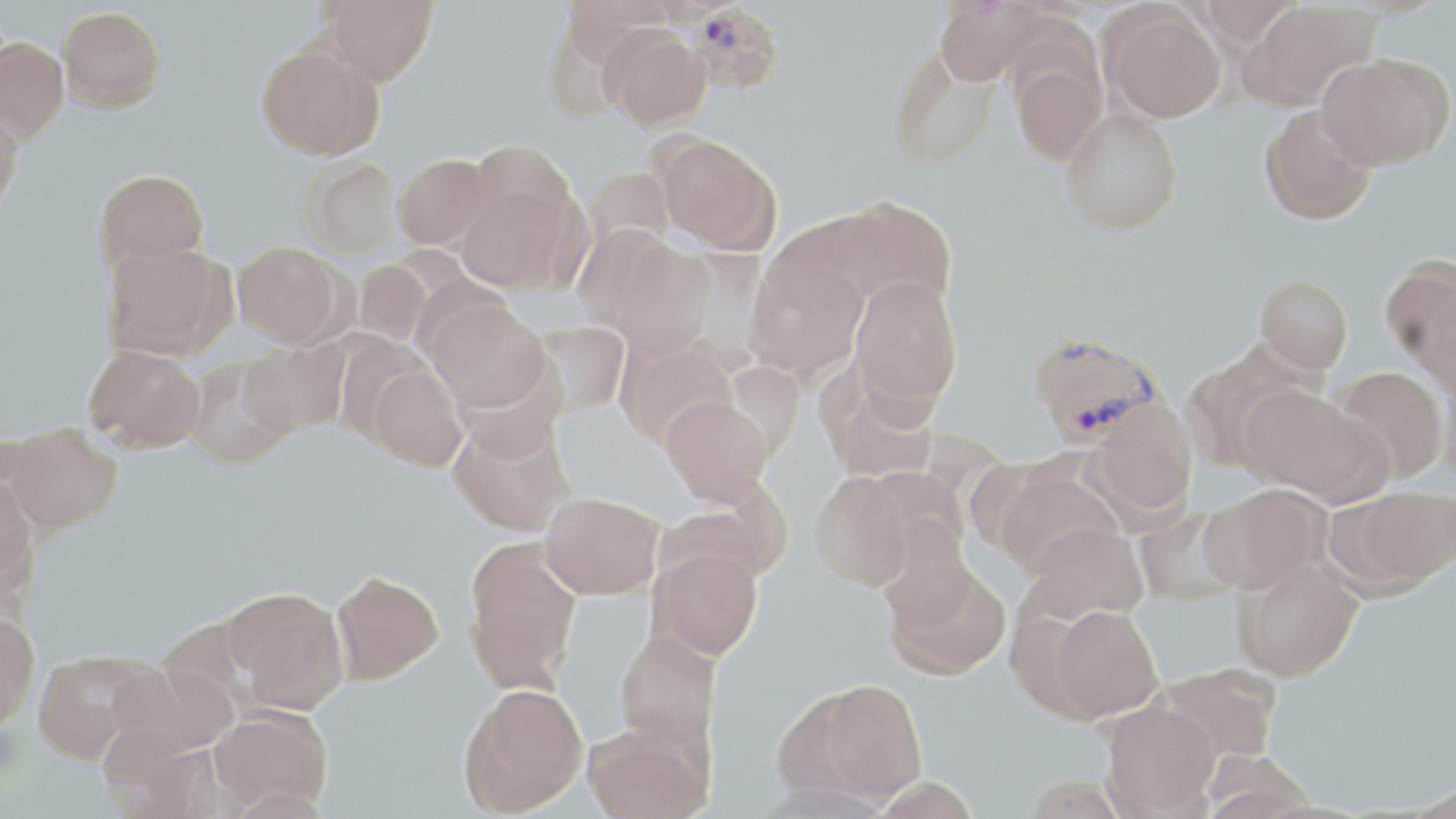

Plasmodium vivax-infected red blood cell locations = approximate bounding boxes as named x1/y1/x2/y2 corners in pixels: (x1=686, y1=3, x2=786, y2=97), (x1=1026, y1=331, x2=1165, y2=449)
slide-level diagnosis = Plasmodium vivax
magnification = 1000x
image size = 1456×819 pixels
stain = May-Grünwald-Giemsa
modality = optical microscopy
preparation = thin blood smear
field of view = one of a larger specimen
uninfected red blood cell locations = approximate bounding boxes as named x1/y1/x2/y2 corners in pixels: (x1=322, y1=0, x2=438, y2=85), (x1=933, y1=0, x2=1042, y2=85), (x1=1193, y1=0, x2=1300, y2=47), (x1=1245, y1=1, x2=1378, y2=109), (x1=57, y1=6, x2=165, y2=112), (x1=1103, y1=7, x2=1225, y2=123), (x1=601, y1=27, x2=711, y2=130), (x1=0, y1=38, x2=69, y2=143), (x1=256, y1=44, x2=383, y2=160), (x1=888, y1=45, x2=997, y2=169), (x1=1317, y1=54, x2=1451, y2=169), (x1=1010, y1=55, x2=1107, y2=166), (x1=0, y1=103, x2=24, y2=217), (x1=1258, y1=105, x2=1377, y2=225), (x1=1061, y1=108, x2=1182, y2=236), (x1=656, y1=135, x2=781, y2=255), (x1=469, y1=139, x2=576, y2=232), (x1=393, y1=153, x2=490, y2=249), (x1=299, y1=156, x2=401, y2=259), (x1=583, y1=166, x2=675, y2=256), (x1=95, y1=168, x2=209, y2=270), (x1=455, y1=184, x2=576, y2=292), (x1=827, y1=198, x2=958, y2=311), (x1=601, y1=236, x2=717, y2=356), (x1=101, y1=241, x2=233, y2=361), (x1=233, y1=241, x2=345, y2=348), (x1=745, y1=257, x2=868, y2=382), (x1=353, y1=260, x2=432, y2=346), (x1=1383, y1=262, x2=1456, y2=387), (x1=849, y1=275, x2=963, y2=415), (x1=1255, y1=275, x2=1353, y2=374), (x1=427, y1=299, x2=550, y2=413), (x1=531, y1=321, x2=629, y2=416), (x1=615, y1=334, x2=739, y2=448), (x1=240, y1=338, x2=349, y2=438), (x1=83, y1=344, x2=206, y2=453), (x1=1179, y1=344, x2=1313, y2=473), (x1=185, y1=356, x2=297, y2=469), (x1=368, y1=365, x2=467, y2=471), (x1=1331, y1=366, x2=1448, y2=483), (x1=818, y1=368, x2=939, y2=484), (x1=1440, y1=377, x2=1456, y2=494), (x1=1241, y1=385, x2=1386, y2=504), (x1=660, y1=393, x2=774, y2=505), (x1=1086, y1=399, x2=1198, y2=520), (x1=448, y1=414, x2=574, y2=537), (x1=3, y1=424, x2=123, y2=533), (x1=993, y1=468, x2=1122, y2=577), (x1=809, y1=471, x2=917, y2=591), (x1=0, y1=474, x2=38, y2=599), (x1=1199, y1=484, x2=1329, y2=595), (x1=1339, y1=487, x2=1456, y2=592), (x1=540, y1=492, x2=664, y2=599), (x1=1134, y1=507, x2=1244, y2=606), (x1=1022, y1=522, x2=1149, y2=622), (x1=462, y1=539, x2=582, y2=693), (x1=650, y1=546, x2=764, y2=659), (x1=882, y1=556, x2=1011, y2=681), (x1=1234, y1=557, x2=1364, y2=682), (x1=331, y1=570, x2=443, y2=684), (x1=225, y1=587, x2=348, y2=714), (x1=1044, y1=604, x2=1164, y2=722), (x1=0, y1=611, x2=39, y2=731), (x1=613, y1=629, x2=722, y2=753), (x1=32, y1=650, x2=157, y2=764), (x1=110, y1=661, x2=238, y2=757), (x1=1155, y1=663, x2=1281, y2=764), (x1=787, y1=678, x2=928, y2=805), (x1=459, y1=683, x2=588, y2=816), (x1=1100, y1=701, x2=1220, y2=818), (x1=209, y1=707, x2=332, y2=814), (x1=96, y1=724, x2=207, y2=818), (x1=583, y1=725, x2=711, y2=819)